Identify the blood parasite species.
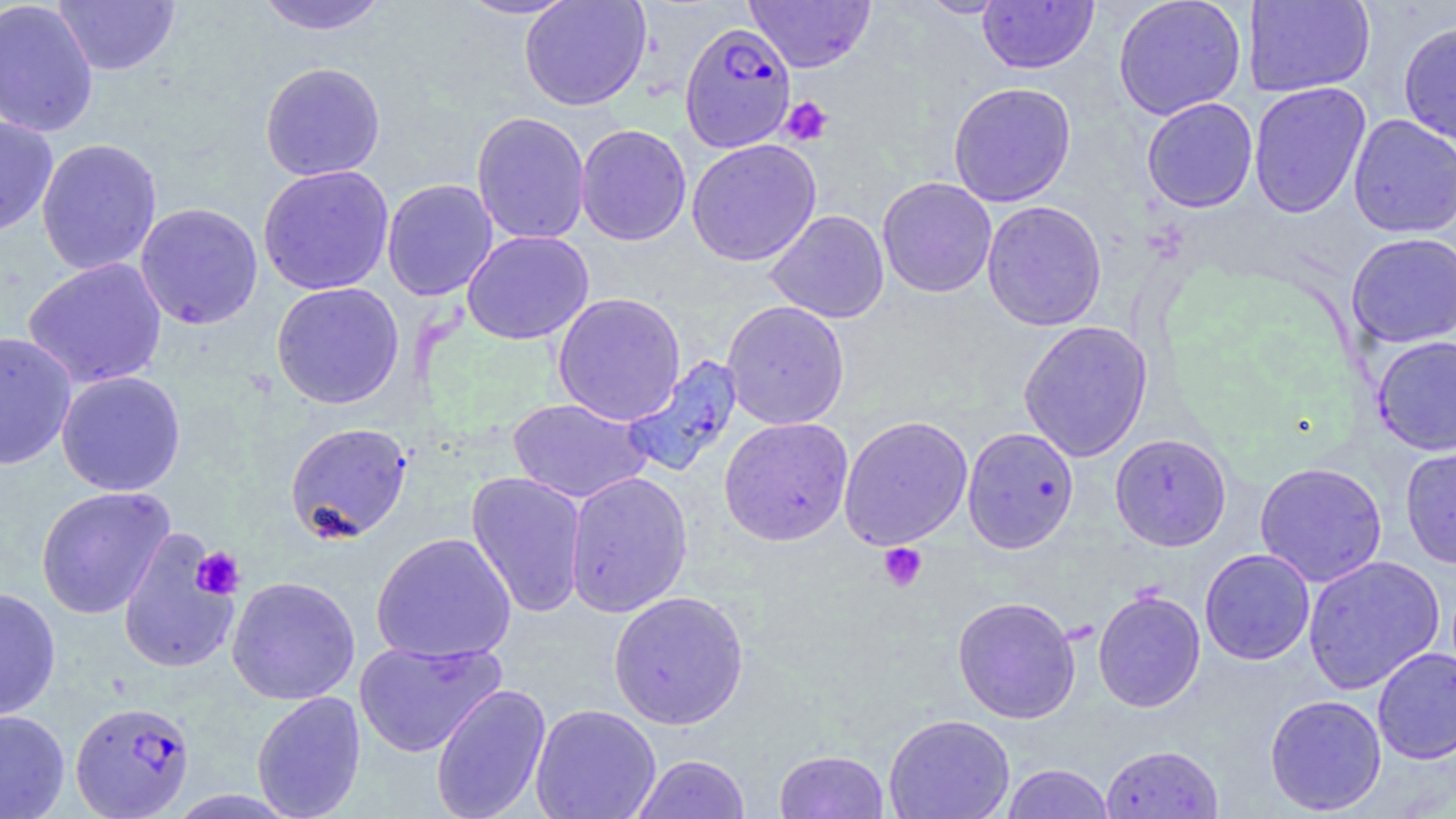

Plasmodium falciparum.

magnification = 1000x
uninfected red blood cell locations = approximate bounding boxes as [x1, y1, x2, y2] in pixels: [0, 0, 99, 138], [254, 0, 390, 36], [455, 0, 579, 20], [519, 0, 651, 111], [918, 0, 1009, 18], [1112, 0, 1247, 120], [1242, 0, 1375, 97], [53, 1, 180, 76], [744, 1, 876, 73], [977, 1, 1098, 74], [1398, 20, 1456, 146], [259, 62, 386, 181], [947, 81, 1077, 207], [1248, 82, 1371, 218], [1142, 97, 1258, 213], [470, 111, 591, 245], [1348, 113, 1456, 238], [0, 115, 58, 236], [575, 124, 692, 246], [36, 138, 162, 276], [686, 138, 822, 267], [257, 164, 395, 295], [877, 177, 997, 298], [381, 178, 498, 301], [981, 200, 1107, 331], [135, 202, 264, 329], [764, 209, 889, 323], [462, 230, 594, 345], [1346, 232, 1456, 347], [22, 257, 168, 389], [270, 282, 405, 409], [552, 292, 686, 426], [721, 300, 850, 430], [1017, 320, 1153, 462], [0, 331, 77, 471], [1372, 336, 1456, 456], [620, 354, 743, 478], [56, 370, 186, 496], [507, 398, 651, 503], [838, 415, 974, 550], [719, 416, 853, 546], [284, 422, 413, 544], [962, 426, 1079, 554], [1110, 433, 1232, 551], [1400, 442, 1456, 569], [1254, 461, 1388, 587], [466, 470, 588, 618], [565, 470, 693, 618], [35, 485, 175, 619], [117, 527, 241, 675], [370, 532, 517, 663], [1199, 548, 1316, 665], [1302, 555, 1445, 694], [226, 575, 361, 705], [0, 587, 61, 721], [1092, 589, 1206, 713], [608, 590, 749, 730], [952, 595, 1081, 724], [353, 639, 507, 758], [1372, 647, 1456, 764], [429, 683, 552, 819], [251, 690, 366, 819], [1264, 694, 1387, 815], [530, 703, 661, 819], [0, 709, 70, 819], [883, 713, 1015, 819], [1100, 744, 1223, 818], [774, 749, 890, 819], [631, 753, 751, 818], [1001, 763, 1115, 818]
Plasmodium falciparum-infected red blood cell locations = approximate bounding boxes as [x1, y1, x2, y2] in pixels: [679, 21, 797, 154], [71, 700, 195, 818]
field of view = one of a larger specimen
modality = optical microscopy
platelet locations = approximate bounding boxes as [x1, y1, x2, y2] in pixels: [779, 96, 834, 146], [878, 542, 927, 592], [191, 547, 245, 600]
preparation = thin blood film
image size = 1456×819 pixels
stain = May-Grünwald-Giemsa